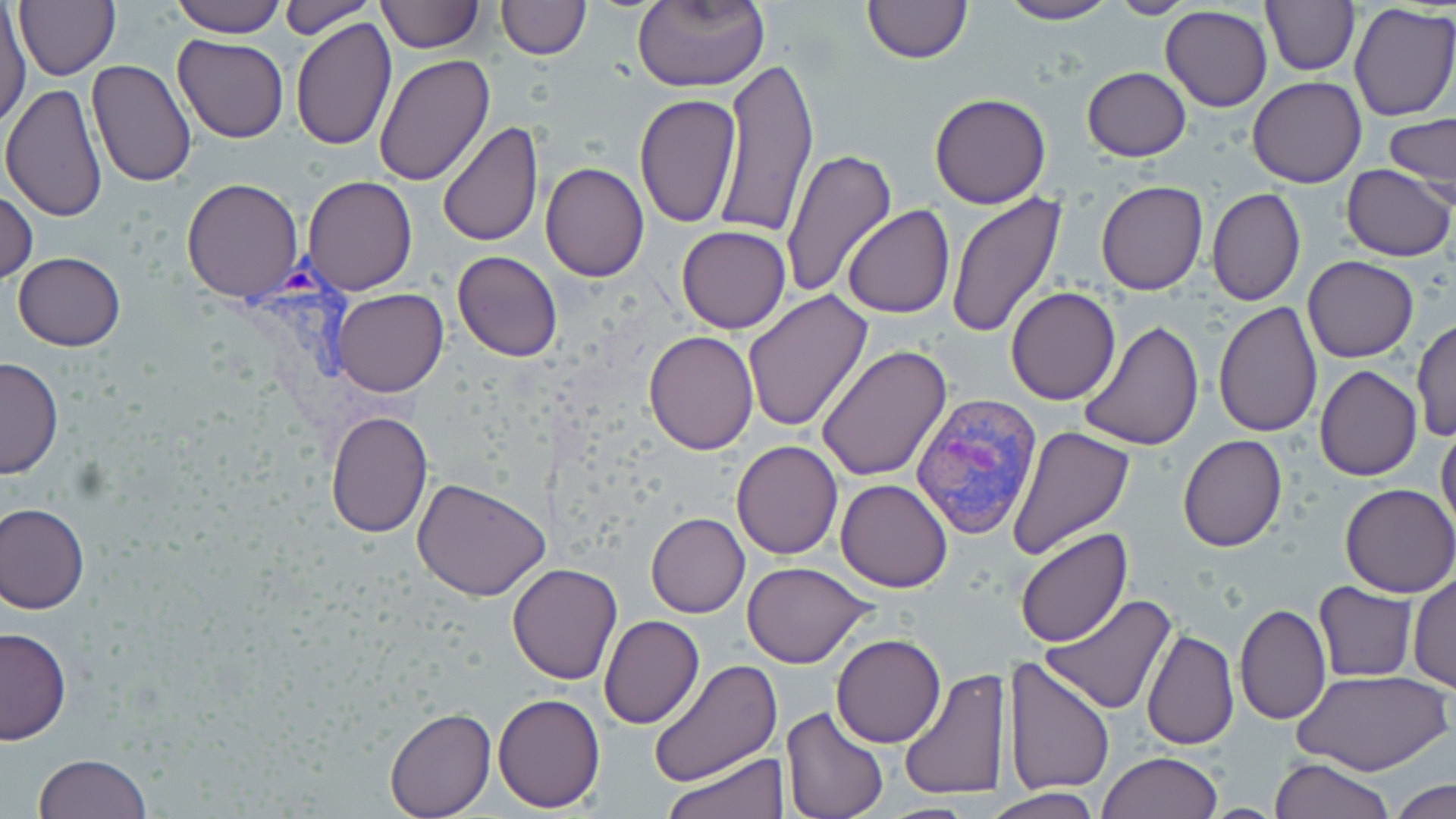

slide-level diagnosis = Plasmodium vivax
uninfected red blood cell locations = approximate bounding boxes as named x1/y1/x2/y2 corners in pixels: (x1=13, y1=0, x2=120, y2=80), (x1=168, y1=0, x2=287, y2=39), (x1=279, y1=0, x2=381, y2=37), (x1=496, y1=0, x2=589, y2=60), (x1=859, y1=0, x2=974, y2=64), (x1=997, y1=0, x2=1117, y2=24), (x1=1109, y1=0, x2=1195, y2=18), (x1=1261, y1=0, x2=1357, y2=76), (x1=375, y1=1, x2=484, y2=53), (x1=631, y1=1, x2=769, y2=91), (x1=1349, y1=3, x2=1456, y2=123), (x1=1159, y1=5, x2=1273, y2=113), (x1=0, y1=8, x2=31, y2=126), (x1=291, y1=18, x2=397, y2=151), (x1=172, y1=34, x2=288, y2=143), (x1=372, y1=53, x2=496, y2=187), (x1=716, y1=55, x2=819, y2=239), (x1=85, y1=60, x2=198, y2=188), (x1=1081, y1=67, x2=1191, y2=161), (x1=1246, y1=77, x2=1367, y2=188), (x1=1, y1=83, x2=107, y2=222), (x1=929, y1=92, x2=1052, y2=209), (x1=633, y1=93, x2=740, y2=230), (x1=1382, y1=112, x2=1456, y2=201), (x1=437, y1=121, x2=543, y2=247), (x1=777, y1=148, x2=897, y2=297), (x1=540, y1=162, x2=649, y2=282), (x1=1340, y1=165, x2=1454, y2=262), (x1=301, y1=175, x2=418, y2=295), (x1=180, y1=177, x2=304, y2=302), (x1=1094, y1=181, x2=1209, y2=294), (x1=1205, y1=187, x2=1306, y2=307), (x1=0, y1=191, x2=37, y2=285), (x1=946, y1=192, x2=1067, y2=339), (x1=841, y1=204, x2=956, y2=318), (x1=676, y1=225, x2=789, y2=333), (x1=451, y1=250, x2=562, y2=362), (x1=12, y1=252, x2=127, y2=352), (x1=1303, y1=255, x2=1418, y2=362), (x1=1006, y1=286, x2=1120, y2=404), (x1=330, y1=288, x2=448, y2=396), (x1=744, y1=289, x2=874, y2=435), (x1=1212, y1=300, x2=1323, y2=436), (x1=643, y1=317, x2=866, y2=445), (x1=1079, y1=320, x2=1204, y2=453), (x1=1412, y1=321, x2=1455, y2=444), (x1=643, y1=331, x2=759, y2=454), (x1=818, y1=346, x2=952, y2=483), (x1=0, y1=356, x2=62, y2=478), (x1=1314, y1=365, x2=1422, y2=483), (x1=325, y1=411, x2=432, y2=538), (x1=1436, y1=423, x2=1456, y2=538), (x1=1006, y1=424, x2=1133, y2=560), (x1=1178, y1=435, x2=1287, y2=552), (x1=731, y1=440, x2=842, y2=561), (x1=413, y1=478, x2=548, y2=603), (x1=835, y1=478, x2=954, y2=593), (x1=1340, y1=483, x2=1455, y2=598), (x1=1, y1=503, x2=89, y2=613), (x1=645, y1=513, x2=749, y2=618), (x1=1015, y1=527, x2=1133, y2=648), (x1=742, y1=561, x2=875, y2=669), (x1=507, y1=563, x2=622, y2=685), (x1=1408, y1=572, x2=1455, y2=693), (x1=1313, y1=580, x2=1417, y2=682), (x1=1040, y1=595, x2=1177, y2=717), (x1=1234, y1=603, x2=1329, y2=724), (x1=599, y1=614, x2=706, y2=729), (x1=541, y1=617, x2=665, y2=761), (x1=0, y1=628, x2=71, y2=744), (x1=1140, y1=629, x2=1239, y2=750), (x1=832, y1=634, x2=945, y2=748), (x1=1001, y1=656, x2=1116, y2=796), (x1=649, y1=660, x2=782, y2=786), (x1=897, y1=667, x2=1010, y2=801), (x1=1293, y1=669, x2=1448, y2=778), (x1=494, y1=691, x2=606, y2=812), (x1=780, y1=707, x2=890, y2=818), (x1=385, y1=708, x2=496, y2=818), (x1=666, y1=751, x2=785, y2=818), (x1=1096, y1=752, x2=1222, y2=819), (x1=32, y1=753, x2=152, y2=819), (x1=1270, y1=756, x2=1394, y2=819), (x1=1388, y1=778, x2=1455, y2=819), (x1=989, y1=786, x2=1101, y2=818)
preparation = thin blood smear
image size = 1456×819 pixels
Plasmodium vivax-infected red blood cell locations = approximate bounding boxes as named x1/y1/x2/y2 corners in pixels: (x1=223, y1=248, x2=428, y2=465), (x1=911, y1=393, x2=1042, y2=542)
magnification = 1000x
field of view = single
modality = optical microscopy
stain = May-Grünwald-Giemsa